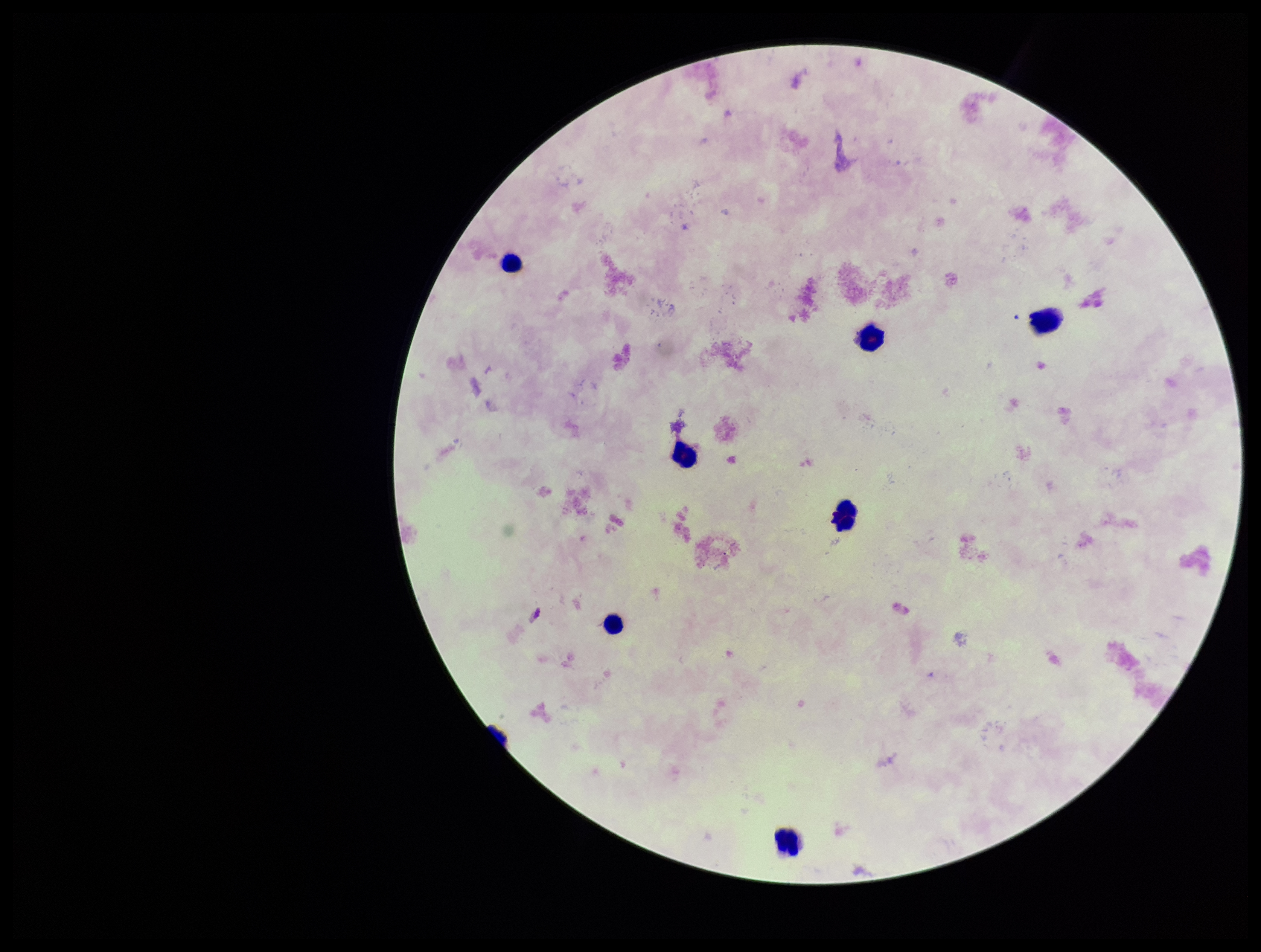

{
  "patient_malaria_status": "negative",
  "stain": "Giemsa",
  "plasmodium_parasites": "none seen",
  "leukocyte_count": 7,
  "capture": "smartphone photograph through the microscope eyepiece",
  "image_size": "1261×952 pixels",
  "preparation": "thick blood smear",
  "field_of_view": "single",
  "parasite_count": 0
}